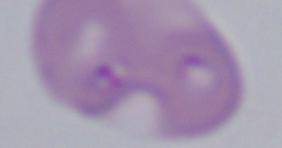
Summary:
  - Modality: photomicrograph
  - Identification: Babesia
  - Magnification: 1000x